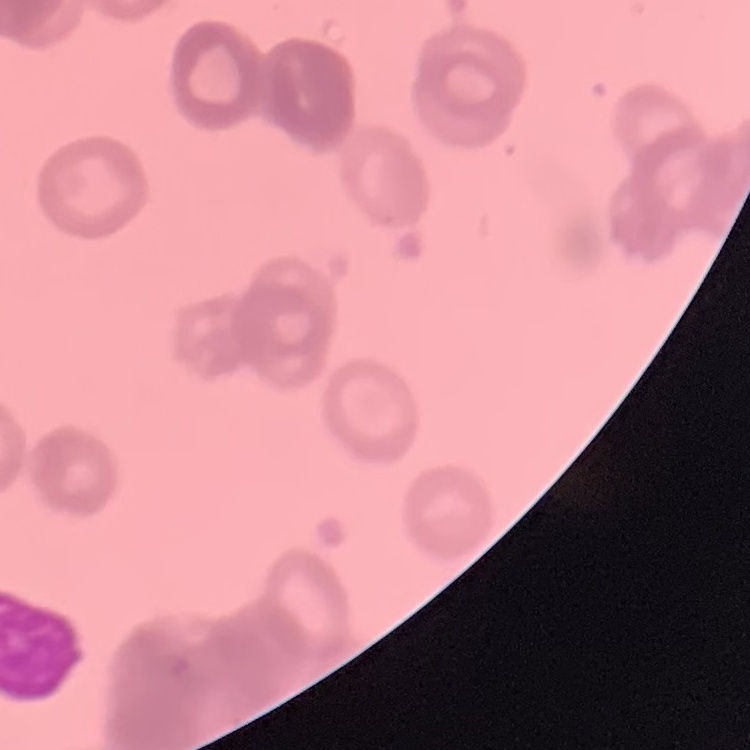 The red blood cells exhibit rouleaux formation. Stained with either Field's or Giemsa. Thin blood smear. Square crop of a larger photomicrograph.